Classify this cell by malaria status.
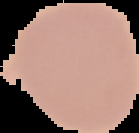
Uninfected.

From a thin blood film. Image is 139×133 pixels. Cell region segmented out of the field of view; the surrounding area is masked to black.